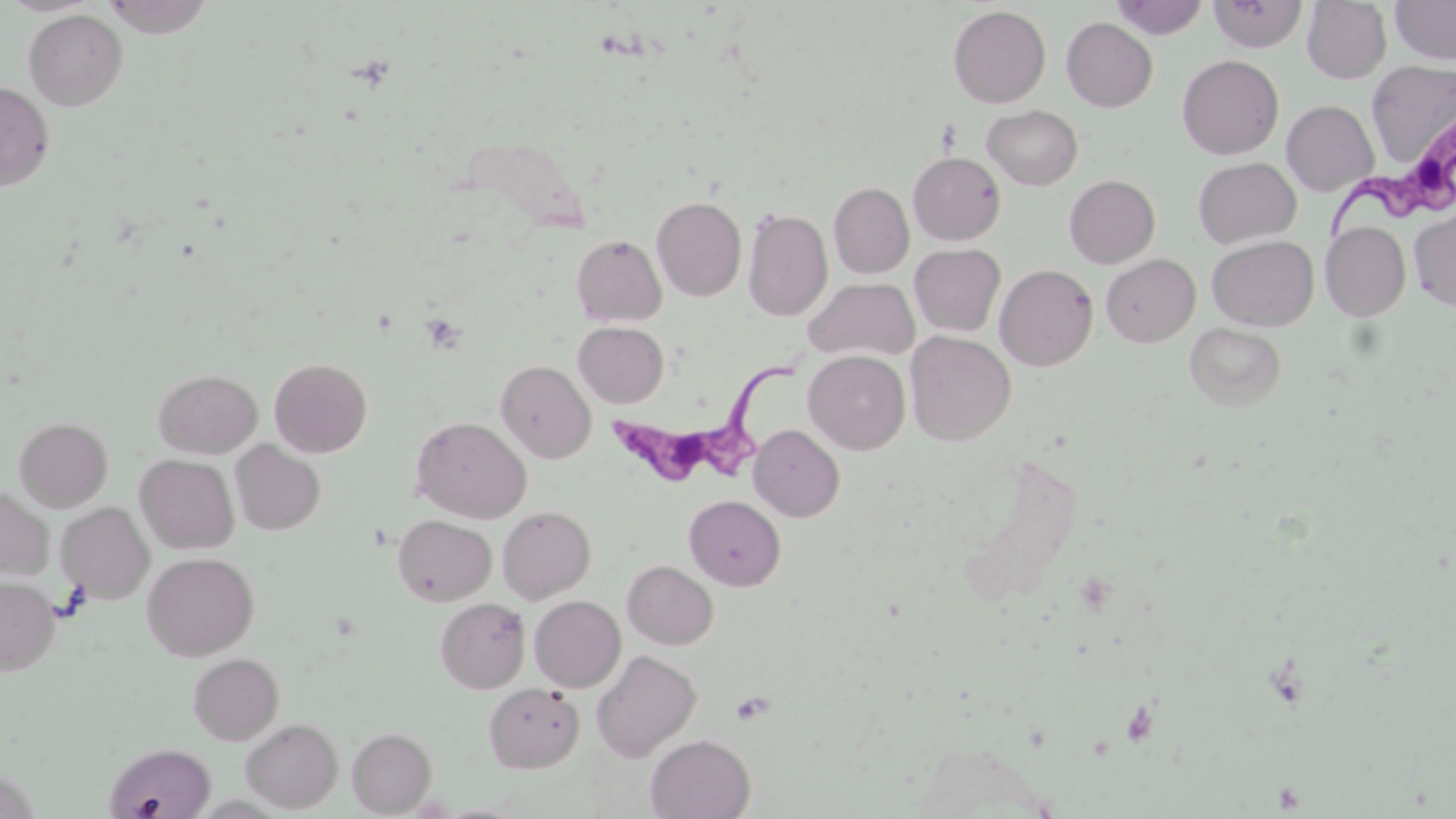
Approximate bounding boxes as (x1, y1, x2, y2) in pixels. Trypanosoma brucei locations: (1326, 131, 1455, 245), (605, 348, 806, 490). Platelet locations: (421, 312, 468, 354). Uninfected red blood cell locations: (101, 0, 217, 37), (1111, 0, 1209, 39), (1209, 0, 1308, 52), (1390, 0, 1456, 65), (1302, 1, 1392, 83), (948, 5, 1051, 108), (23, 9, 128, 110), (1062, 17, 1158, 112), (1177, 54, 1284, 159), (1366, 61, 1456, 166), (0, 80, 55, 190), (1282, 100, 1378, 197), (982, 104, 1083, 190), (909, 151, 1006, 245), (1193, 157, 1301, 248), (1064, 174, 1160, 268), (829, 182, 914, 278), (652, 195, 747, 302), (743, 207, 832, 322), (1410, 208, 1456, 311), (1321, 222, 1410, 320), (571, 234, 667, 326), (1207, 236, 1318, 330), (909, 243, 1006, 337), (1101, 254, 1200, 347), (995, 264, 1098, 371), (804, 277, 920, 362), (574, 322, 669, 408), (1185, 323, 1286, 411), (905, 331, 1016, 445), (804, 350, 910, 454), (269, 357, 373, 458), (495, 360, 596, 463), (153, 369, 262, 457), (14, 416, 113, 511), (411, 416, 531, 523), (749, 424, 844, 521), (231, 442, 325, 535), (135, 454, 239, 554), (0, 487, 56, 582), (684, 495, 785, 590), (56, 502, 153, 603), (498, 506, 595, 603), (393, 515, 496, 605), (142, 552, 259, 661), (623, 561, 718, 650), (0, 577, 60, 675), (529, 595, 626, 692), (435, 597, 529, 693), (591, 649, 701, 762), (188, 653, 284, 744), (483, 682, 584, 772), (241, 719, 342, 812), (347, 727, 437, 816), (645, 734, 756, 818), (107, 742, 217, 817). Slide-level diagnosis: Trypanosoma brucei. Image is 1456×819 pixels. 1000x magnification. Optical microscopy. May-Grünwald-Giemsa stain. Thin blood film. Single field of view.